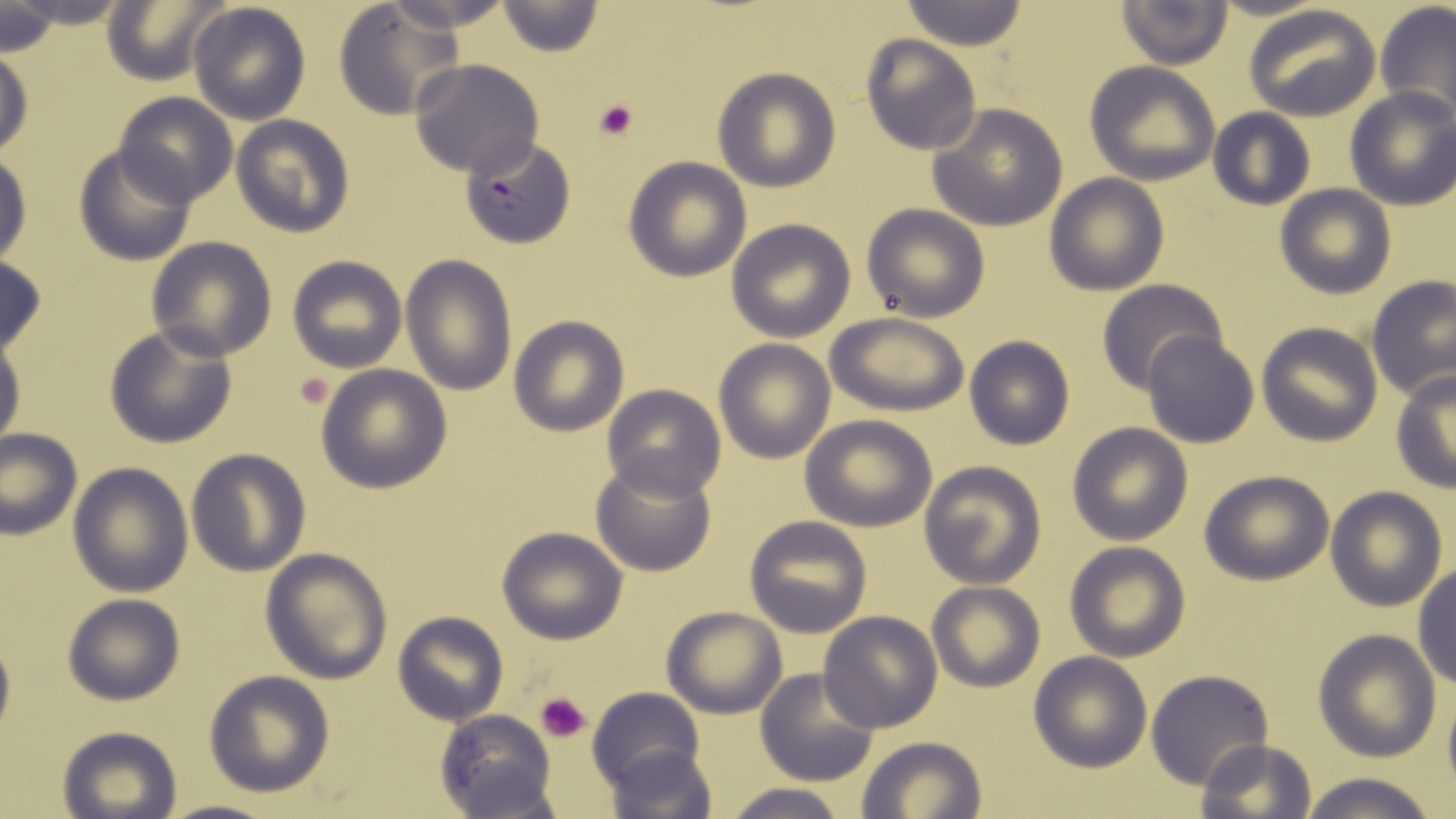
slide-level diagnosis = Plasmodium falciparum
modality = light microscopy
preparation = thin blood film
platelet locations = approximate bounding boxes as (x1, y1, x2, y2) in pixels: (591, 96, 643, 143), (294, 370, 336, 410), (535, 690, 592, 741)
Plasmodium falciparum-infected red blood cell locations = approximate bounding boxes as (x1, y1, x2, y2) in pixels: (460, 136, 577, 247)
uninfected red blood cell locations = approximate bounding boxes as (x1, y1, x2, y2) in pixels: (3, 0, 137, 29), (187, 0, 311, 123), (383, 0, 512, 31), (1376, 0, 1456, 122), (898, 1, 1029, 48), (1115, 1, 1234, 70), (98, 2, 231, 83), (332, 2, 465, 121), (494, 2, 604, 56), (1243, 4, 1382, 121), (0, 5, 60, 53), (861, 34, 982, 155), (0, 46, 32, 161), (408, 58, 544, 178), (1085, 61, 1220, 184), (712, 66, 840, 192), (1344, 88, 1456, 210), (111, 92, 239, 207), (927, 103, 1069, 232), (1207, 109, 1315, 210), (232, 114, 355, 238), (74, 144, 197, 266), (0, 152, 32, 268), (623, 156, 752, 281), (1044, 173, 1168, 294), (1274, 184, 1397, 299), (861, 202, 990, 322), (725, 217, 856, 341), (144, 236, 277, 360), (0, 253, 47, 361), (402, 253, 517, 398), (286, 255, 409, 373), (1364, 276, 1456, 402), (1096, 279, 1227, 394), (826, 312, 970, 416), (508, 316, 629, 436), (1255, 322, 1383, 446), (103, 323, 237, 450), (1143, 330, 1259, 448), (964, 336, 1074, 450), (0, 338, 25, 452), (714, 340, 834, 462), (316, 365, 452, 493), (1391, 370, 1456, 492), (601, 384, 726, 500), (800, 415, 938, 531), (1068, 422, 1191, 545), (0, 429, 81, 538), (186, 448, 311, 577), (590, 456, 717, 577), (917, 461, 1045, 589), (68, 462, 194, 596), (1199, 469, 1335, 585), (1326, 486, 1447, 611), (744, 516, 871, 637), (497, 527, 628, 644), (1064, 541, 1191, 662), (260, 547, 394, 685), (1412, 563, 1456, 689), (927, 581, 1045, 692), (62, 593, 185, 706), (660, 605, 787, 719), (392, 610, 509, 725), (818, 611, 944, 733), (0, 623, 14, 747), (1312, 630, 1441, 762), (1028, 652, 1153, 771), (756, 667, 881, 786), (204, 669, 334, 796), (1145, 670, 1274, 790), (588, 687, 707, 791), (433, 709, 557, 817), (58, 726, 181, 818), (856, 736, 986, 819), (1197, 739, 1318, 819), (605, 743, 717, 819), (1297, 772, 1443, 819), (723, 781, 847, 819)
image size = 1456×819 pixels
field of view = single
magnification = 1000x
stain = May-Grünwald-Giemsa